Locate every white blood cell.
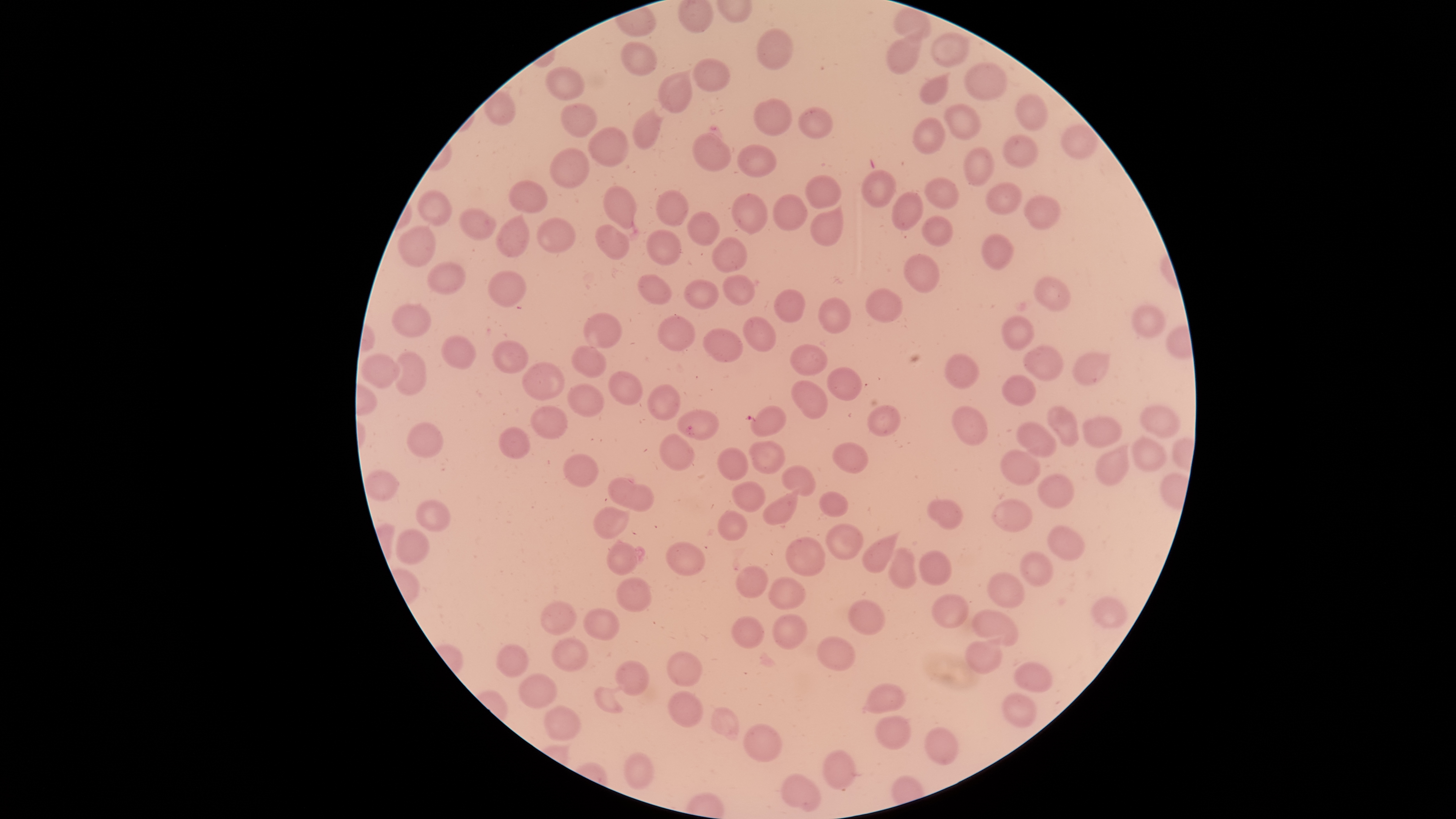
No white blood cells identified.

{
  "presence": "malaria parasites seen",
  "stain": "Giemsa",
  "species": "Plasmodium falciparum",
  "parasitized_red_blood_cells": "approximate bounding boxes, in pixels from the top-left corner: (left=678, top=410, right=718, bottom=440)",
  "visible_region": "circular",
  "uninfected_red_blood_cells": "approximate bounding boxes, in pixels from the top-left corner: (left=894, top=8, right=933, bottom=42), (left=758, top=30, right=794, bottom=69), (left=932, top=30, right=968, bottom=68), (left=888, top=34, right=925, bottom=74), (left=622, top=43, right=657, bottom=76), (left=694, top=59, right=729, bottom=92), (left=964, top=64, right=1007, bottom=101), (left=547, top=68, right=584, bottom=100), (left=659, top=73, right=691, bottom=113), (left=919, top=76, right=949, bottom=105), (left=1015, top=96, right=1047, bottom=131), (left=755, top=101, right=792, bottom=135), (left=562, top=105, right=596, bottom=138), (left=946, top=105, right=980, bottom=139), (left=798, top=110, right=835, bottom=142), (left=633, top=112, right=662, bottom=149), (left=915, top=119, right=945, bottom=154), (left=1062, top=126, right=1097, bottom=159), (left=589, top=128, right=628, bottom=168), (left=692, top=133, right=731, bottom=173), (left=1003, top=135, right=1039, bottom=169), (left=737, top=145, right=777, bottom=178), (left=963, top=147, right=994, bottom=186), (left=551, top=148, right=589, bottom=191), (left=862, top=172, right=896, bottom=206), (left=925, top=177, right=959, bottom=211), (left=807, top=178, right=842, bottom=208), (left=509, top=181, right=548, bottom=213), (left=986, top=183, right=1021, bottom=215), (left=604, top=187, right=638, bottom=230), (left=657, top=190, right=689, bottom=226), (left=418, top=191, right=452, bottom=226), (left=892, top=192, right=925, bottom=229), (left=732, top=193, right=767, bottom=235), (left=774, top=195, right=807, bottom=230), (left=1024, top=196, right=1059, bottom=229), (left=460, top=209, right=495, bottom=240), (left=688, top=212, right=719, bottom=246), (left=811, top=212, right=845, bottom=247), (left=498, top=215, right=532, bottom=257), (left=922, top=216, right=953, bottom=246), (left=537, top=218, right=575, bottom=254), (left=596, top=225, right=630, bottom=260), (left=398, top=226, right=436, bottom=267), (left=648, top=230, right=681, bottom=266), (left=983, top=234, right=1013, bottom=270), (left=712, top=237, right=748, bottom=272), (left=905, top=255, right=940, bottom=292), (left=427, top=263, right=467, bottom=294), (left=489, top=272, right=524, bottom=308), (left=637, top=275, right=671, bottom=305), (left=721, top=276, right=755, bottom=306), (left=1034, top=276, right=1070, bottom=310), (left=683, top=280, right=719, bottom=310), (left=773, top=289, right=806, bottom=322), (left=866, top=289, right=902, bottom=323), (left=818, top=298, right=851, bottom=335), (left=392, top=304, right=432, bottom=338), (left=1133, top=307, right=1165, bottom=338), (left=585, top=314, right=622, bottom=349), (left=658, top=315, right=694, bottom=351), (left=743, top=317, right=776, bottom=353), (left=1003, top=317, right=1033, bottom=351), (left=705, top=329, right=743, bottom=362), (left=440, top=335, right=475, bottom=371), (left=492, top=340, right=528, bottom=374), (left=792, top=345, right=827, bottom=375), (left=572, top=346, right=606, bottom=378), (left=1023, top=347, right=1062, bottom=380), (left=393, top=352, right=427, bottom=396), (left=1074, top=354, right=1108, bottom=385), (left=945, top=356, right=979, bottom=389), (left=361, top=357, right=399, bottom=387), (left=521, top=363, right=566, bottom=402), (left=828, top=367, right=862, bottom=402), (left=609, top=372, right=642, bottom=405), (left=1002, top=376, right=1035, bottom=405), (left=792, top=379, right=828, bottom=419), (left=568, top=384, right=604, bottom=417), (left=649, top=384, right=679, bottom=419), (left=867, top=405, right=900, bottom=437), (left=531, top=406, right=567, bottom=440), (left=751, top=406, right=786, bottom=437), (left=953, top=406, right=986, bottom=446), (left=1142, top=406, right=1175, bottom=438), (left=1046, top=408, right=1079, bottom=446), (left=1083, top=417, right=1122, bottom=448), (left=1018, top=423, right=1056, bottom=457), (left=406, top=424, right=443, bottom=460), (left=501, top=428, right=530, bottom=459), (left=659, top=435, right=694, bottom=471), (left=1134, top=438, right=1165, bottom=470), (left=747, top=441, right=784, bottom=474), (left=834, top=442, right=869, bottom=474), (left=1096, top=446, right=1135, bottom=485), (left=717, top=449, right=747, bottom=481), (left=1002, top=452, right=1041, bottom=485), (left=565, top=453, right=598, bottom=488), (left=782, top=466, right=817, bottom=497), (left=365, top=470, right=400, bottom=501), (left=1040, top=475, right=1074, bottom=508), (left=609, top=481, right=653, bottom=511), (left=733, top=481, right=765, bottom=511), (left=762, top=493, right=798, bottom=526), (left=820, top=493, right=847, bottom=517), (left=992, top=500, right=1033, bottom=532), (left=416, top=501, right=451, bottom=533), (left=929, top=501, right=962, bottom=530), (left=593, top=510, right=626, bottom=540), (left=717, top=511, right=748, bottom=541), (left=829, top=525, right=862, bottom=561), (left=1048, top=526, right=1085, bottom=561), (left=396, top=528, right=427, bottom=565), (left=863, top=537, right=899, bottom=572), (left=785, top=538, right=825, bottom=576), (left=607, top=541, right=637, bottom=575), (left=667, top=541, right=704, bottom=576), (left=889, top=547, right=918, bottom=588), (left=1021, top=550, right=1053, bottom=587), (left=919, top=551, right=952, bottom=588), (left=736, top=567, right=769, bottom=599), (left=989, top=572, right=1024, bottom=607), (left=617, top=577, right=652, bottom=613), (left=767, top=578, right=804, bottom=611), (left=933, top=594, right=970, bottom=628), (left=1094, top=598, right=1125, bottom=629), (left=848, top=600, right=884, bottom=635), (left=541, top=603, right=576, bottom=635), (left=583, top=608, right=620, bottom=641), (left=972, top=611, right=1017, bottom=647), (left=773, top=615, right=806, bottom=650), (left=732, top=617, right=765, bottom=649), (left=816, top=636, right=857, bottom=669), (left=553, top=639, right=589, bottom=671), (left=967, top=641, right=1001, bottom=674), (left=498, top=646, right=528, bottom=677), (left=666, top=652, right=703, bottom=688), (left=617, top=662, right=650, bottom=697), (left=1014, top=664, right=1050, bottom=694), (left=520, top=674, right=557, bottom=711), (left=863, top=685, right=902, bottom=712), (left=594, top=686, right=623, bottom=715), (left=669, top=692, right=703, bottom=727), (left=1004, top=695, right=1036, bottom=728), (left=546, top=708, right=581, bottom=740), (left=711, top=709, right=739, bottom=736), (left=875, top=718, right=910, bottom=749), (left=744, top=724, right=781, bottom=761), (left=924, top=727, right=958, bottom=766), (left=823, top=750, right=855, bottom=791), (left=624, top=754, right=652, bottom=790), (left=780, top=775, right=821, bottom=812)",
  "image_size": "1456×819 pixels",
  "preparation": "thin smear of blood",
  "capture": "smartphone photograph through the microscope eyepiece",
  "field_of_view": "single"
}